Identify the parasite.
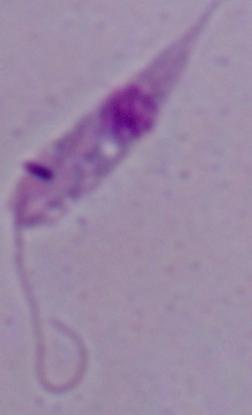

This is Leishmania.

magnification = 1000x
modality = photomicrograph